Report the malaria status of this cell.
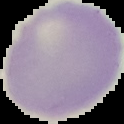
It is uninfected.

Cell region segmented out of the field of view; the surrounding area is masked to black. Image is 124×124 pixels. From a thin blood smear.